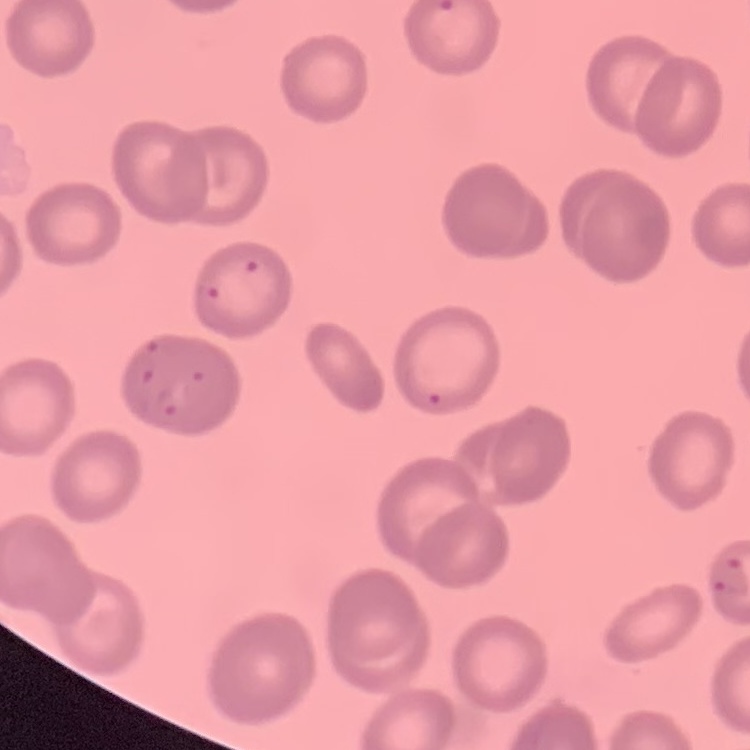

red blood cell morphology = no rouleaux formation
stain = Field's or Giemsa
preparation = thin peripheral smear
image type = one tile cut from a larger photomicrograph